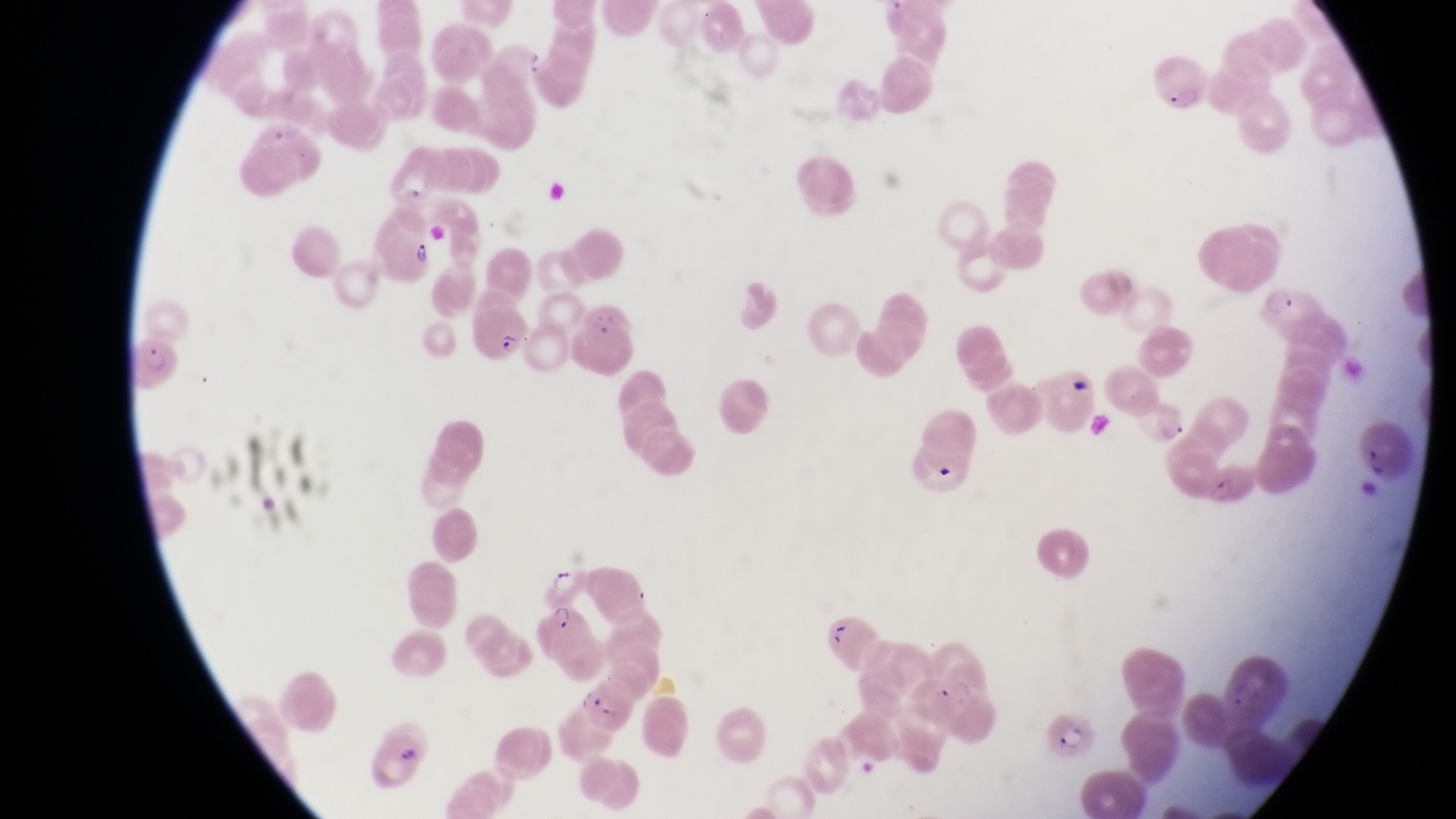
Approximate bounding boxes as [left, top, right, bottom] in pixels.
Summary:
  - Trophozoite locations: [547, 565, 579, 597]
  - Parasitised red blood cell locations: [1149, 60, 1213, 118], [373, 221, 437, 282], [1264, 281, 1333, 345], [475, 298, 534, 362], [581, 309, 642, 378], [133, 340, 188, 399], [1144, 400, 1190, 443], [532, 602, 596, 660], [582, 679, 635, 738], [1050, 706, 1099, 759]
  - Artifact (platelet-like body, stain precipitate, or debris) locations: [930, 459, 962, 486], [830, 621, 857, 651]
  - Magnification: 1000x
  - Image size: 1456×819 pixels
  - Capture: smartphone photograph through the eyepiece of an Olympus CX-23 microscope
  - Preparation: thin blood film
  - Country: Uganda
  - Field of view: single